Report the malaria status of this cell.
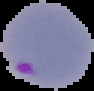

It is parasitized.

Summary:
  - Preparation: thin blood smear
  - Image type: cell region segmented out of the field of view; surrounding area masked to black
  - Image size: 94×91 pixels